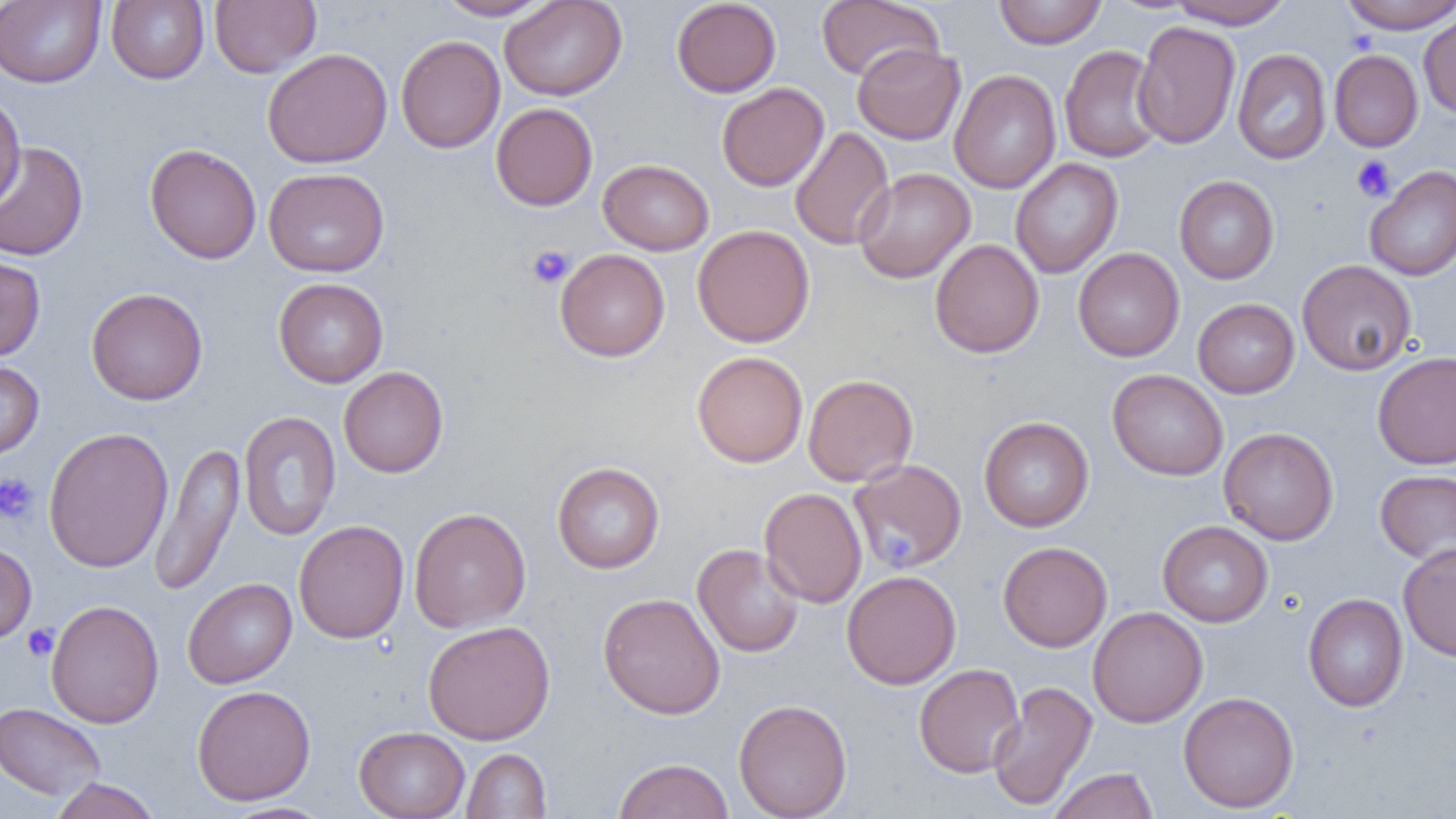
{
  "slide_level_diagnosis": "no evidence of blood parasites",
  "platelet_locations": "approximate bounding boxes as [x1, y1, x2, y2] in pixels: [1351, 155, 1396, 201], [526, 245, 574, 288], [0, 472, 39, 524], [875, 521, 920, 565], [22, 624, 59, 661]",
  "field_of_view": "single",
  "uninfected_red_blood_cell_locations": "approximate bounding boxes as [x1, y1, x2, y2] in pixels: [0, 0, 106, 88], [106, 0, 209, 84], [210, 0, 321, 78], [435, 0, 554, 20], [499, 0, 626, 100], [671, 0, 781, 97], [816, 0, 943, 82], [994, 0, 1106, 49], [1339, 0, 1456, 33], [1167, 1, 1294, 29], [1418, 9, 1456, 119], [1133, 20, 1241, 149], [396, 35, 505, 153], [852, 43, 965, 145], [1059, 45, 1166, 163], [262, 48, 393, 169], [1233, 48, 1331, 164], [1329, 49, 1423, 152], [949, 69, 1061, 194], [717, 82, 829, 191], [0, 89, 26, 212], [491, 103, 598, 211], [790, 126, 895, 251], [0, 141, 89, 261], [145, 143, 262, 264], [1010, 158, 1123, 279], [598, 159, 714, 255], [1365, 165, 1456, 281], [263, 167, 389, 277], [853, 168, 975, 283], [1174, 175, 1279, 284], [692, 224, 815, 347], [930, 238, 1044, 358], [1072, 247, 1185, 362], [555, 248, 670, 361], [0, 254, 45, 362], [1297, 260, 1417, 375], [273, 277, 388, 388], [86, 287, 208, 405], [1192, 298, 1300, 398], [692, 351, 808, 467], [1372, 351, 1456, 470], [0, 360, 44, 460], [339, 366, 448, 478], [1107, 369, 1228, 480], [803, 374, 918, 487], [238, 410, 341, 541], [979, 416, 1094, 532], [43, 426, 173, 572], [1219, 427, 1339, 545], [149, 440, 245, 597], [847, 458, 968, 574], [552, 462, 664, 573], [1375, 469, 1456, 565], [759, 487, 867, 608], [408, 508, 531, 633], [294, 519, 409, 644], [1158, 520, 1273, 627], [0, 541, 36, 643], [997, 541, 1112, 652], [692, 543, 805, 658], [1398, 543, 1456, 662], [841, 570, 961, 689], [183, 578, 297, 688], [598, 592, 725, 719], [1303, 593, 1408, 712], [45, 599, 164, 728], [1088, 606, 1208, 727], [423, 620, 555, 745], [914, 663, 1025, 778], [987, 680, 1098, 811], [192, 684, 316, 806], [1178, 691, 1299, 813], [733, 698, 852, 819], [0, 702, 106, 801], [354, 726, 470, 819], [461, 748, 551, 818], [613, 758, 734, 819], [1049, 767, 1158, 819], [48, 778, 162, 819], [218, 802, 335, 819]",
  "modality": "optical microscopy",
  "image_size": "1456×819 pixels",
  "preparation": "thin blood smear",
  "magnification": "1000x"
}